State which parasite is depicted.
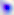
Toxoplasma gondii.

modality = micrograph
magnification = 400x